Report the malaria status of this cell.
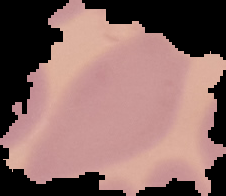
Uninfected.

preparation = thin blood film
image type = segmented cell region with the area outside set to black
image size = 226×196 pixels